Outline each Babesia divergens-infected red blood cell.
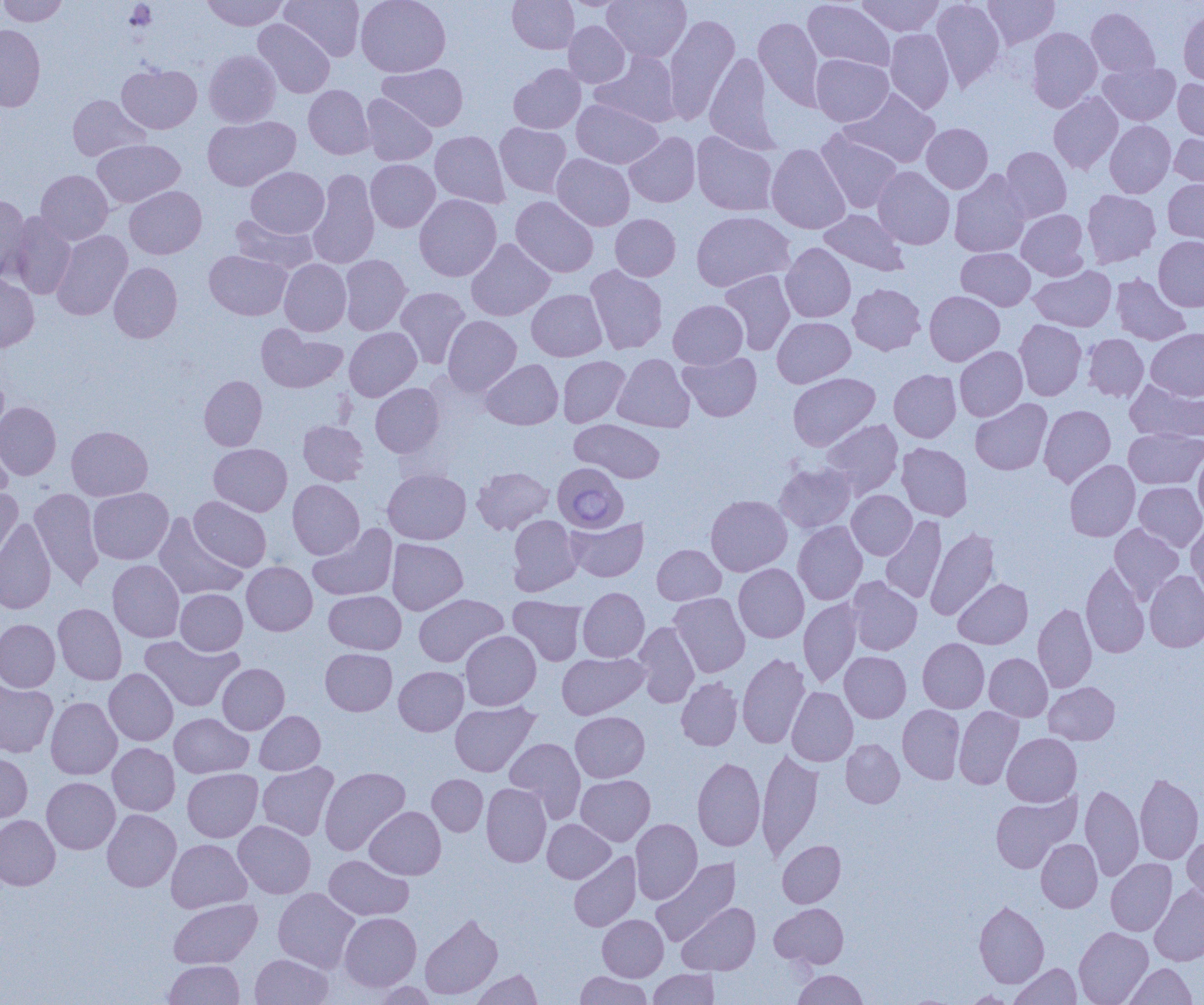
Approximate bounding boxes as (x1, y1, x2, y2) in pixels.
Babesia divergens-infected red blood cells: (555, 467, 625, 532).

Platelet locations: (124, 2, 156, 30). Uninfected red blood cell locations: (0, 0, 68, 26), (201, 0, 288, 30), (281, 0, 364, 61), (356, 0, 451, 77), (508, 0, 579, 54), (603, 0, 691, 62), (803, 0, 895, 72), (856, 0, 944, 36), (931, 0, 1006, 91), (983, 0, 1059, 48), (1086, 7, 1160, 79), (1179, 9, 1204, 86), (664, 14, 740, 125), (754, 16, 824, 110), (253, 19, 335, 98), (564, 20, 630, 88), (0, 24, 45, 111), (1027, 27, 1102, 112), (885, 28, 954, 114), (204, 50, 281, 127), (591, 50, 680, 127), (704, 52, 778, 154), (810, 54, 893, 126), (1098, 62, 1180, 125), (378, 63, 468, 131), (509, 63, 586, 134), (117, 64, 202, 134), (1173, 78, 1204, 141), (303, 84, 374, 159), (842, 89, 940, 167), (1048, 92, 1123, 174), (67, 94, 150, 161), (361, 94, 437, 166), (572, 99, 663, 168), (202, 116, 300, 191), (1105, 120, 1176, 198), (495, 122, 572, 197), (921, 123, 993, 193), (816, 129, 902, 214), (430, 131, 510, 208), (692, 131, 778, 216), (625, 132, 700, 207), (1169, 132, 1204, 190), (92, 139, 185, 207), (766, 144, 850, 234), (1001, 146, 1071, 222), (552, 153, 634, 231), (366, 159, 440, 232), (246, 166, 329, 238), (872, 166, 955, 249), (306, 169, 380, 269), (36, 170, 113, 244), (948, 170, 1030, 258), (1163, 178, 1204, 246), (125, 186, 207, 259), (1082, 190, 1161, 267), (414, 194, 501, 281), (0, 196, 32, 283), (511, 196, 598, 277), (818, 208, 909, 276), (1016, 209, 1089, 279), (690, 210, 794, 292), (9, 212, 76, 299), (611, 214, 680, 281), (229, 215, 317, 274), (51, 230, 133, 320), (1154, 236, 1204, 311), (466, 239, 555, 321), (781, 243, 856, 322), (957, 247, 1035, 311), (204, 250, 292, 320), (340, 254, 411, 335), (279, 259, 351, 336), (109, 262, 182, 342), (585, 264, 668, 354), (1029, 265, 1116, 332), (719, 269, 795, 355), (0, 273, 39, 352), (1111, 274, 1191, 345), (848, 283, 926, 355), (395, 287, 470, 368), (526, 289, 607, 361), (925, 290, 1005, 366), (668, 300, 748, 369), (442, 315, 521, 396), (772, 316, 856, 387), (1014, 319, 1087, 400), (256, 323, 347, 393), (345, 327, 422, 401), (1146, 328, 1204, 401), (1083, 333, 1148, 402), (954, 346, 1027, 421), (678, 351, 762, 421), (613, 354, 695, 432), (558, 355, 630, 427), (481, 359, 563, 429), (889, 369, 961, 442), (0, 371, 9, 441), (788, 372, 880, 451), (199, 375, 267, 450), (1125, 379, 1204, 442), (370, 383, 444, 457), (971, 398, 1052, 475), (0, 401, 61, 480), (1039, 404, 1115, 487), (570, 419, 665, 483), (820, 419, 903, 499), (298, 420, 368, 485), (0, 424, 14, 501), (66, 425, 153, 501), (1124, 429, 1203, 489), (896, 442, 972, 521), (209, 443, 292, 516), (1193, 447, 1204, 523), (1065, 459, 1141, 541), (774, 462, 856, 533), (472, 466, 554, 534), (383, 468, 471, 544), (287, 480, 364, 559), (1134, 482, 1204, 551), (30, 487, 104, 589), (0, 488, 23, 566), (88, 488, 173, 564), (847, 490, 917, 560), (705, 494, 792, 576), (189, 496, 271, 571), (154, 514, 247, 601), (508, 515, 581, 595), (565, 516, 648, 582), (880, 516, 947, 603), (1185, 516, 1204, 602), (0, 518, 56, 615), (793, 521, 867, 605), (1109, 523, 1184, 603), (308, 524, 398, 601), (925, 527, 1000, 620), (387, 538, 468, 615), (652, 544, 725, 605), (107, 560, 184, 642), (1081, 560, 1149, 659), (242, 561, 317, 635), (733, 563, 809, 642), (1144, 570, 1204, 652), (846, 577, 922, 655), (953, 578, 1033, 649), (578, 587, 650, 662), (175, 589, 247, 655), (324, 590, 406, 654), (669, 592, 750, 677), (414, 593, 508, 667), (508, 596, 587, 666), (798, 599, 862, 688), (1033, 602, 1097, 692), (53, 603, 127, 685), (0, 619, 60, 692), (633, 621, 700, 708), (460, 631, 541, 710), (140, 636, 243, 712), (917, 638, 989, 713), (320, 648, 397, 716), (839, 651, 911, 722), (557, 652, 649, 719), (737, 652, 810, 748), (984, 653, 1052, 721), (217, 663, 289, 735), (393, 666, 468, 736), (104, 668, 178, 746), (676, 676, 742, 750), (0, 681, 58, 757), (1044, 682, 1119, 745), (787, 686, 857, 766), (46, 696, 122, 779), (450, 701, 540, 776), (897, 705, 965, 784), (954, 706, 1024, 789), (254, 710, 325, 775), (570, 711, 649, 782), (169, 712, 253, 778), (1002, 733, 1081, 807), (505, 737, 585, 820), (841, 739, 904, 808), (108, 743, 180, 815), (756, 747, 824, 860), (0, 752, 32, 822), (692, 757, 765, 851), (257, 762, 339, 840), (319, 767, 410, 855), (182, 768, 262, 842), (1135, 773, 1203, 865), (427, 774, 488, 836), (576, 775, 655, 845), (42, 777, 120, 854), (481, 782, 551, 867), (1080, 784, 1143, 881), (990, 790, 1081, 874), (365, 806, 446, 879), (102, 809, 181, 891), (0, 815, 60, 890), (543, 819, 615, 883), (630, 819, 702, 904), (233, 820, 315, 898), (1182, 834, 1204, 908), (167, 839, 251, 913), (1036, 839, 1102, 913), (777, 840, 845, 908), (569, 851, 641, 931), (324, 854, 413, 920), (650, 857, 740, 947), (1106, 858, 1177, 936), (1149, 884, 1204, 966), (273, 887, 359, 973), (168, 898, 262, 968), (974, 901, 1049, 988), (677, 902, 760, 975), (770, 903, 848, 968), (339, 912, 421, 991), (420, 913, 503, 1000), (598, 914, 668, 981), (1074, 927, 1153, 1005), (250, 953, 333, 1005), (163, 960, 244, 1005), (1009, 962, 1081, 1005), (1124, 963, 1196, 1004), (471, 968, 542, 1005), (648, 968, 719, 1005), (793, 970, 867, 1005), (575, 971, 652, 1005), (371, 981, 438, 1004), (963, 991, 1017, 1004). Slide-level diagnosis: Babesia divergens. Thin blood smear. 1000x magnification. Single field of view. Optical microscopy. Image is 1204×1005 pixels.